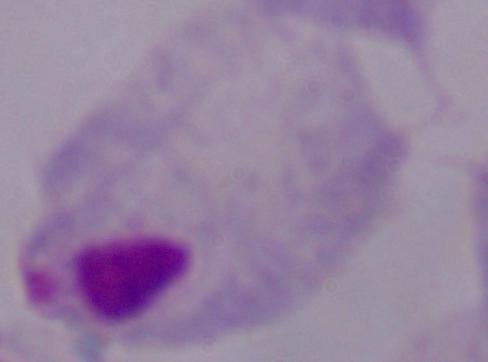
A trichomonad is shown. 1000x magnification. Micrograph.